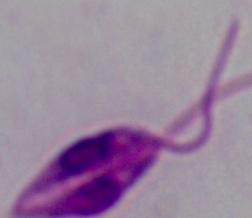

Summary:
  - Identification: Leishmania
  - Magnification: 1000x
  - Modality: micrograph